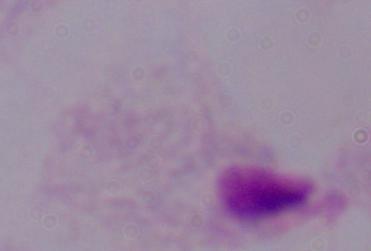

identification: trichomonad
magnification: 1000x
modality: micrograph